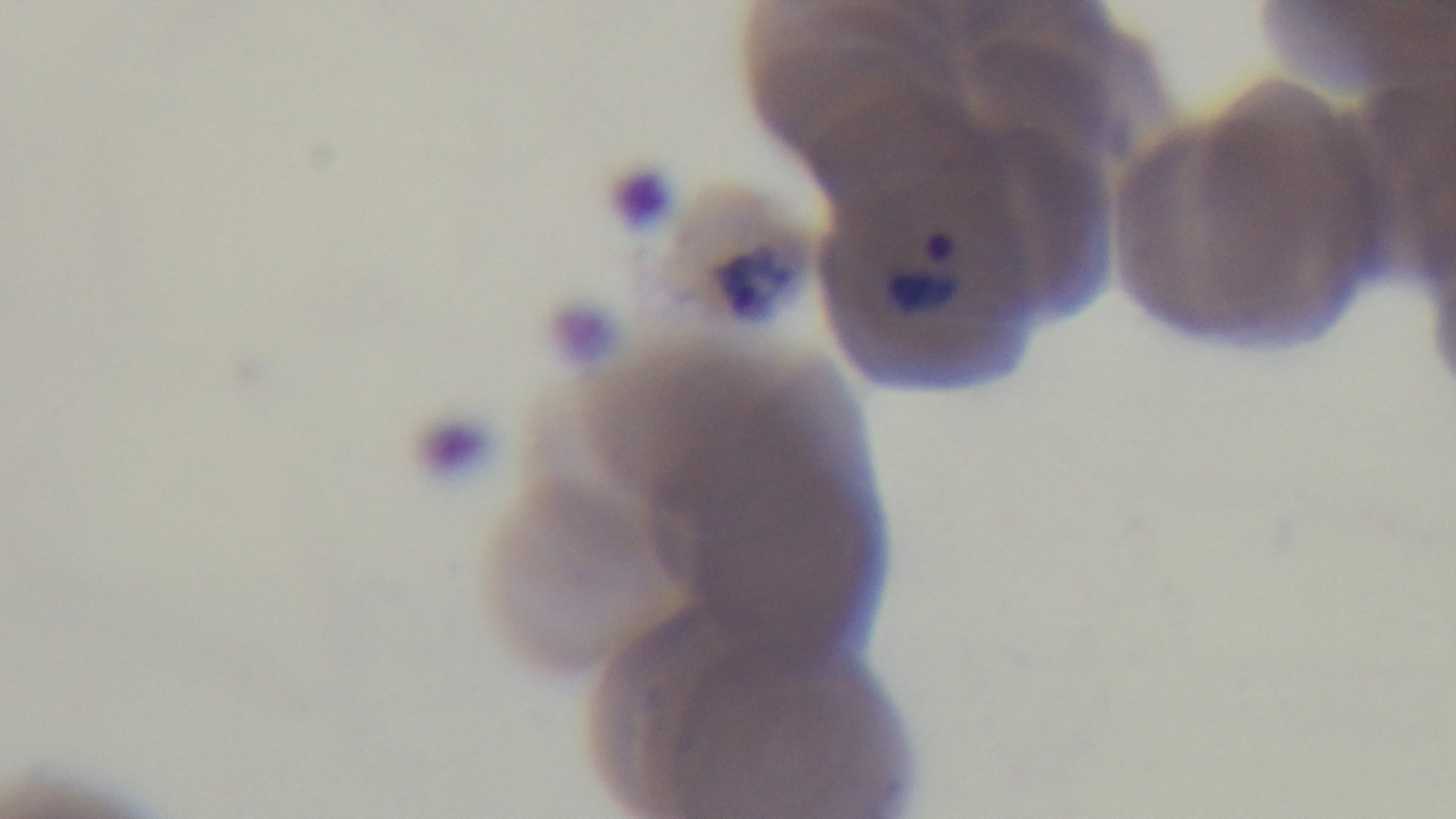
Summary:
  - Capture: mounted 4K digital camera
  - Objective: 100x oil immersion
  - Malaria status: infected
  - Field of view: single
  - Modality: light microscopy
  - Stain: Giemsa
  - Preparation: thin blood film